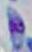

1000x magnification. Photomicrograph. Toxoplasma gondii is seen.